Point out Plasmodium parasites and leukocytes.
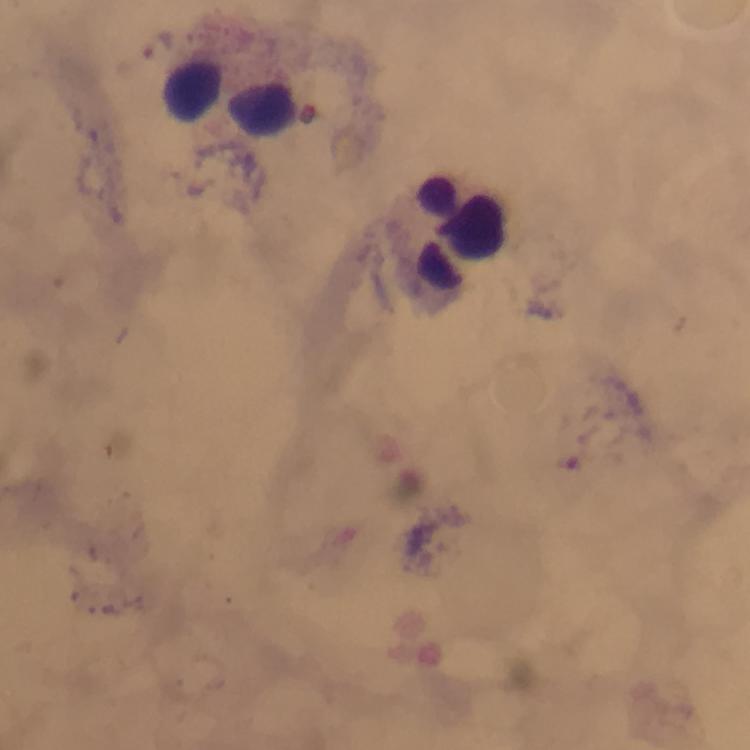
No Plasmodium parasites seen.
Approximate centers as (x, y) in pixels.
Leukocytes: (234, 97), (452, 233).

Summary:
  - Stain: Giemsa
  - Cropped from: a single field of view
  - Preparation: thick smear
  - Capture: smartphone camera through the microscope
  - Immersion oil: used
  - Magnification: 100x
  - Context: from a malaria diagnostic workup
  - Image size: 750×750 pixels